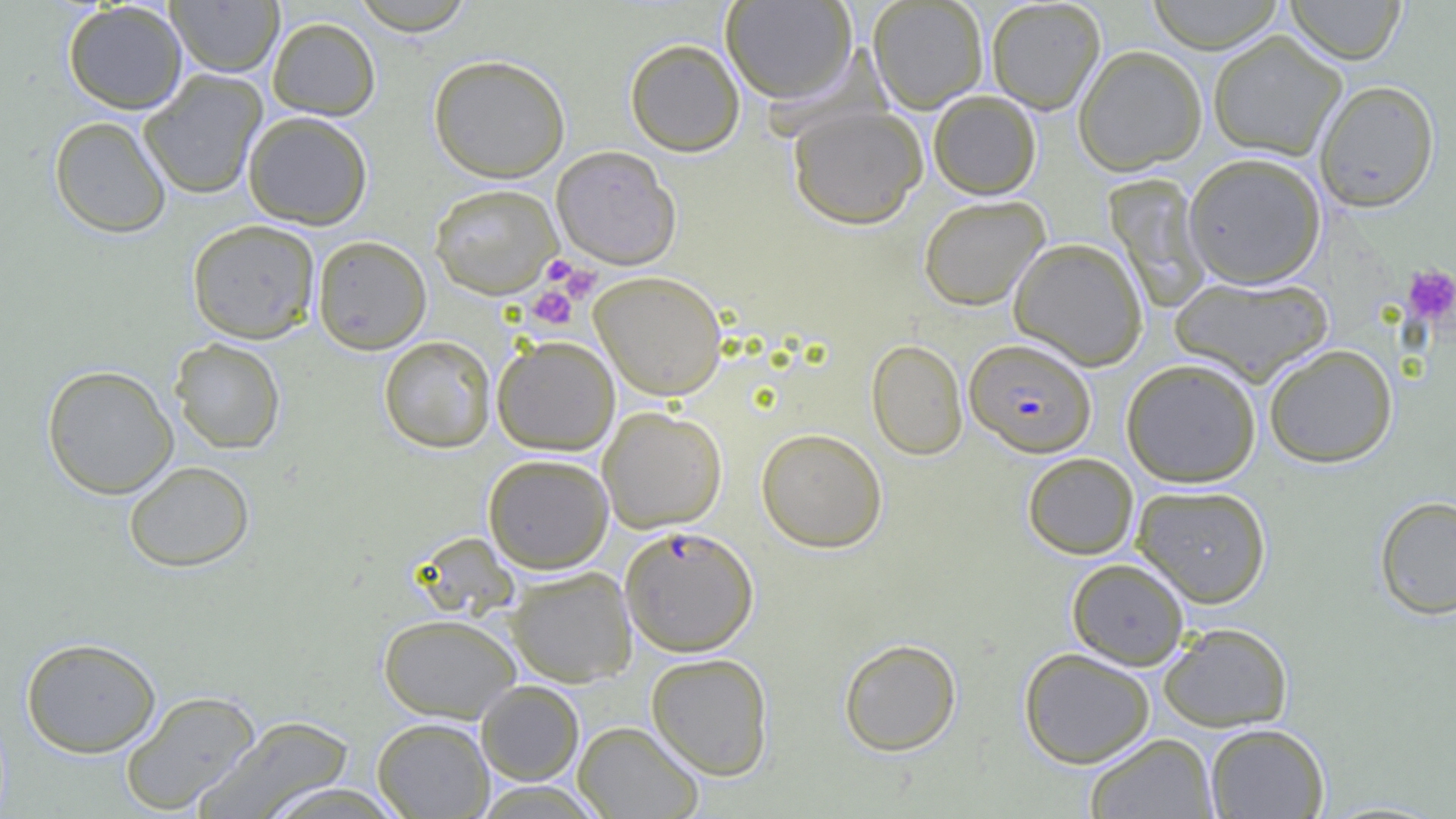

Summary:
  - Coordinate format: approximate bounding boxes as named x1/y1/x2/y2 corners in pixels
  - Platelet locations: (x1=541, y1=255, x2=583, y2=287), (x1=555, y1=261, x2=601, y2=303), (x1=1402, y1=264, x2=1456, y2=325), (x1=526, y1=286, x2=578, y2=330)
  - Plasmodium falciparum-infected red blood cell locations: (x1=965, y1=338, x2=1096, y2=457), (x1=619, y1=525, x2=759, y2=656)
  - Uninfected red blood cell locations: (x1=166, y1=0, x2=283, y2=77), (x1=348, y1=0, x2=478, y2=35), (x1=720, y1=0, x2=857, y2=103), (x1=868, y1=0, x2=988, y2=112), (x1=986, y1=0, x2=1106, y2=114), (x1=1145, y1=0, x2=1285, y2=53), (x1=1286, y1=0, x2=1405, y2=65), (x1=63, y1=1, x2=188, y2=114), (x1=267, y1=16, x2=381, y2=121), (x1=1208, y1=29, x2=1347, y2=161), (x1=625, y1=38, x2=745, y2=156), (x1=1073, y1=45, x2=1207, y2=175), (x1=428, y1=54, x2=571, y2=182), (x1=139, y1=69, x2=268, y2=200), (x1=1315, y1=79, x2=1440, y2=212), (x1=928, y1=90, x2=1041, y2=200), (x1=788, y1=106, x2=927, y2=229), (x1=243, y1=111, x2=373, y2=230), (x1=48, y1=116, x2=172, y2=238), (x1=551, y1=146, x2=681, y2=269), (x1=1183, y1=152, x2=1326, y2=288), (x1=1105, y1=174, x2=1212, y2=312), (x1=429, y1=183, x2=562, y2=299), (x1=918, y1=195, x2=1049, y2=311), (x1=186, y1=219, x2=320, y2=343), (x1=312, y1=235, x2=432, y2=354), (x1=1010, y1=237, x2=1148, y2=369), (x1=590, y1=271, x2=728, y2=400), (x1=1170, y1=276, x2=1333, y2=384), (x1=378, y1=335, x2=496, y2=453), (x1=492, y1=336, x2=620, y2=455), (x1=169, y1=337, x2=286, y2=454), (x1=867, y1=338, x2=968, y2=460), (x1=1263, y1=343, x2=1398, y2=468), (x1=1121, y1=358, x2=1261, y2=487), (x1=41, y1=364, x2=178, y2=499), (x1=598, y1=405, x2=727, y2=532), (x1=756, y1=427, x2=887, y2=552), (x1=1023, y1=452, x2=1138, y2=559), (x1=483, y1=454, x2=614, y2=573), (x1=123, y1=460, x2=255, y2=573), (x1=1133, y1=484, x2=1271, y2=607), (x1=1375, y1=495, x2=1456, y2=619), (x1=1067, y1=558, x2=1189, y2=669), (x1=506, y1=566, x2=637, y2=687), (x1=378, y1=614, x2=522, y2=722), (x1=1159, y1=622, x2=1293, y2=731), (x1=21, y1=637, x2=161, y2=757), (x1=838, y1=638, x2=962, y2=756), (x1=1019, y1=647, x2=1155, y2=768), (x1=646, y1=652, x2=774, y2=780), (x1=475, y1=680, x2=585, y2=785), (x1=120, y1=690, x2=261, y2=815), (x1=195, y1=715, x2=356, y2=819), (x1=371, y1=717, x2=494, y2=818), (x1=573, y1=721, x2=704, y2=819), (x1=1205, y1=723, x2=1330, y2=819), (x1=1085, y1=732, x2=1219, y2=819), (x1=258, y1=781, x2=407, y2=819)
  - Slide-level diagnosis: Plasmodium falciparum
  - Field of view: single
  - Magnification: 1000x
  - Image size: 1456×819 pixels
  - Modality: optical microscopy
  - Preparation: thin blood smear